Assess this cell for malaria.
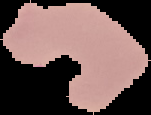
It is parasitized.

From a thin blood film. Cell region segmented out of the field of view; the surrounding area is masked to black. Image is 151×115 pixels.